State which parasite is depicted.
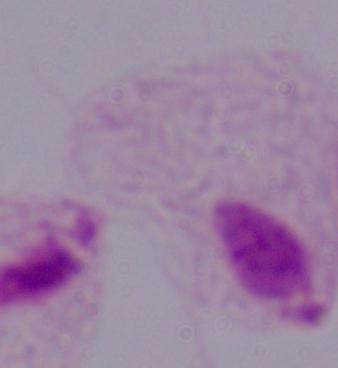
This is a trichomonad.

Photomicrograph. 1000x magnification.